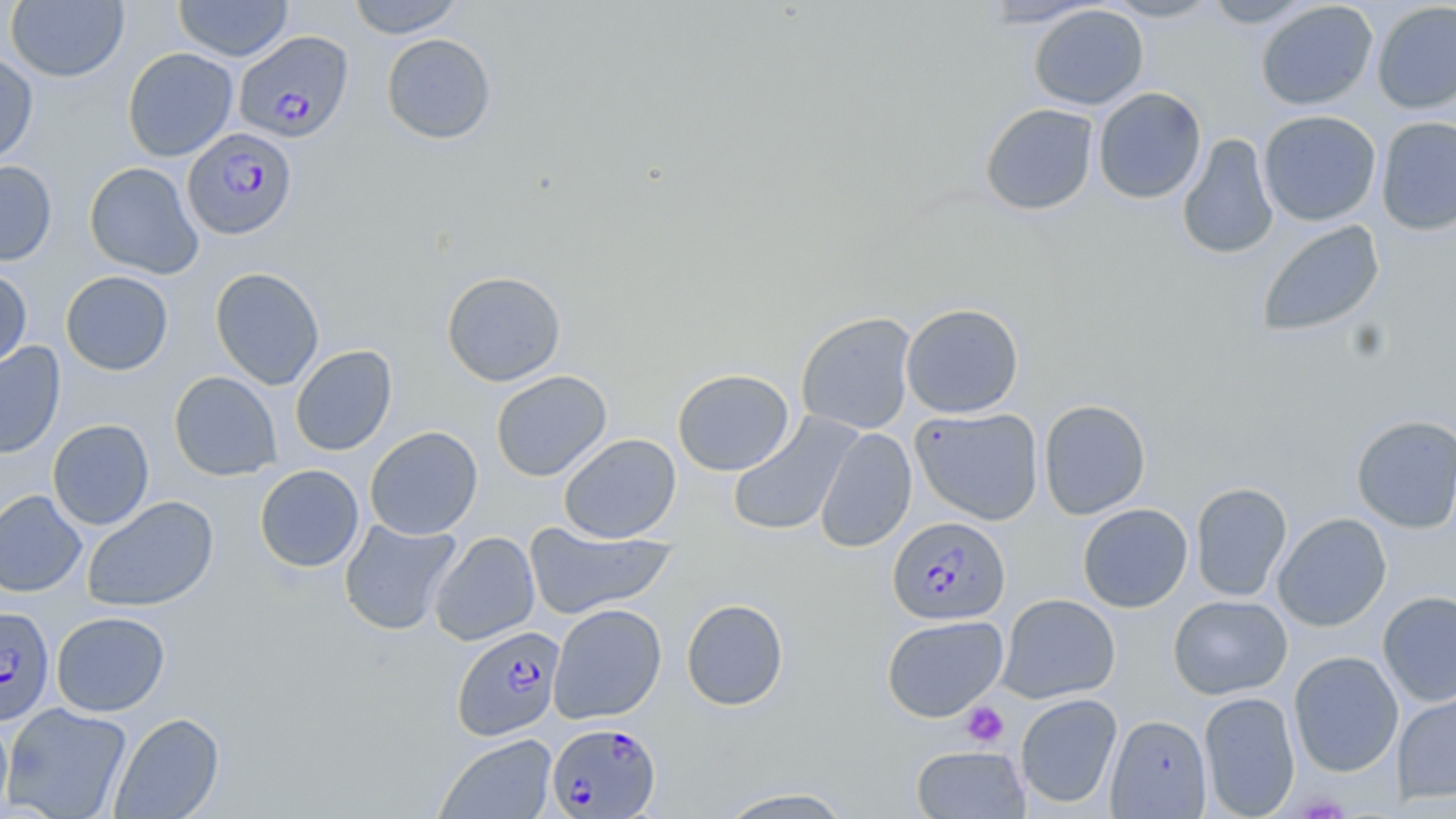
Summary:
  - Coordinate format: approximate bounding boxes as [x1, y1, x2, y2] in pixels
  - Platelet locations: [960, 701, 1009, 747]
  - Uninfected red blood cell locations: [346, 0, 466, 38], [976, 0, 1107, 27], [1101, 0, 1223, 22], [1201, 0, 1318, 28], [6, 1, 129, 83], [173, 1, 293, 61], [1255, 1, 1378, 110], [1372, 1, 1456, 114], [1028, 4, 1149, 110], [381, 33, 497, 144], [122, 47, 238, 162], [0, 50, 38, 165], [1093, 86, 1207, 204], [979, 103, 1099, 215], [1259, 110, 1381, 226], [1376, 116, 1456, 236], [1177, 133, 1278, 260], [0, 160, 58, 266], [84, 161, 204, 279], [1257, 219, 1385, 337], [210, 266, 325, 390], [0, 267, 33, 373], [60, 270, 173, 376], [441, 270, 566, 387], [901, 302, 1024, 418], [795, 311, 917, 435], [0, 341, 66, 459], [290, 345, 397, 456], [672, 368, 794, 476], [490, 370, 612, 482], [168, 371, 282, 481], [1038, 398, 1151, 520], [910, 407, 1044, 525], [728, 413, 861, 536], [1351, 414, 1456, 533], [48, 419, 155, 530], [364, 426, 483, 540], [814, 427, 917, 553], [559, 433, 681, 543], [254, 464, 364, 572], [1190, 482, 1292, 602], [0, 490, 87, 597], [82, 495, 219, 613], [1077, 503, 1193, 613], [1272, 512, 1392, 632], [339, 518, 462, 635], [524, 521, 675, 620], [429, 531, 540, 646], [1378, 590, 1456, 707], [997, 594, 1120, 703], [1168, 594, 1292, 700], [681, 598, 789, 711], [548, 603, 667, 724], [51, 611, 170, 716], [882, 615, 1008, 722], [1288, 651, 1404, 777], [1392, 690, 1456, 804], [1198, 691, 1300, 818], [1015, 693, 1122, 810], [1, 702, 133, 819], [110, 712, 225, 819], [0, 713, 14, 819], [1106, 714, 1212, 818], [435, 733, 557, 818], [911, 745, 1030, 818], [714, 786, 857, 818]
  - Plasmodium falciparum-infected red blood cell locations: [234, 31, 354, 142], [182, 127, 297, 240], [888, 517, 1011, 625], [0, 606, 55, 725], [452, 625, 565, 740], [547, 722, 661, 818]
  - Slide-level diagnosis: Plasmodium falciparum
  - Magnification: 1000x
  - Stain: May-Grünwald-Giemsa
  - Field of view: one of a larger specimen
  - Image size: 1456×819 pixels
  - Preparation: thin blood smear
  - Modality: light microscopy